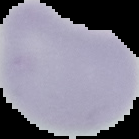
The area outside the segmented cell region is set to black. Image is 139×139 pixels. Result: no malaria parasites detected. From a thin blood smear.